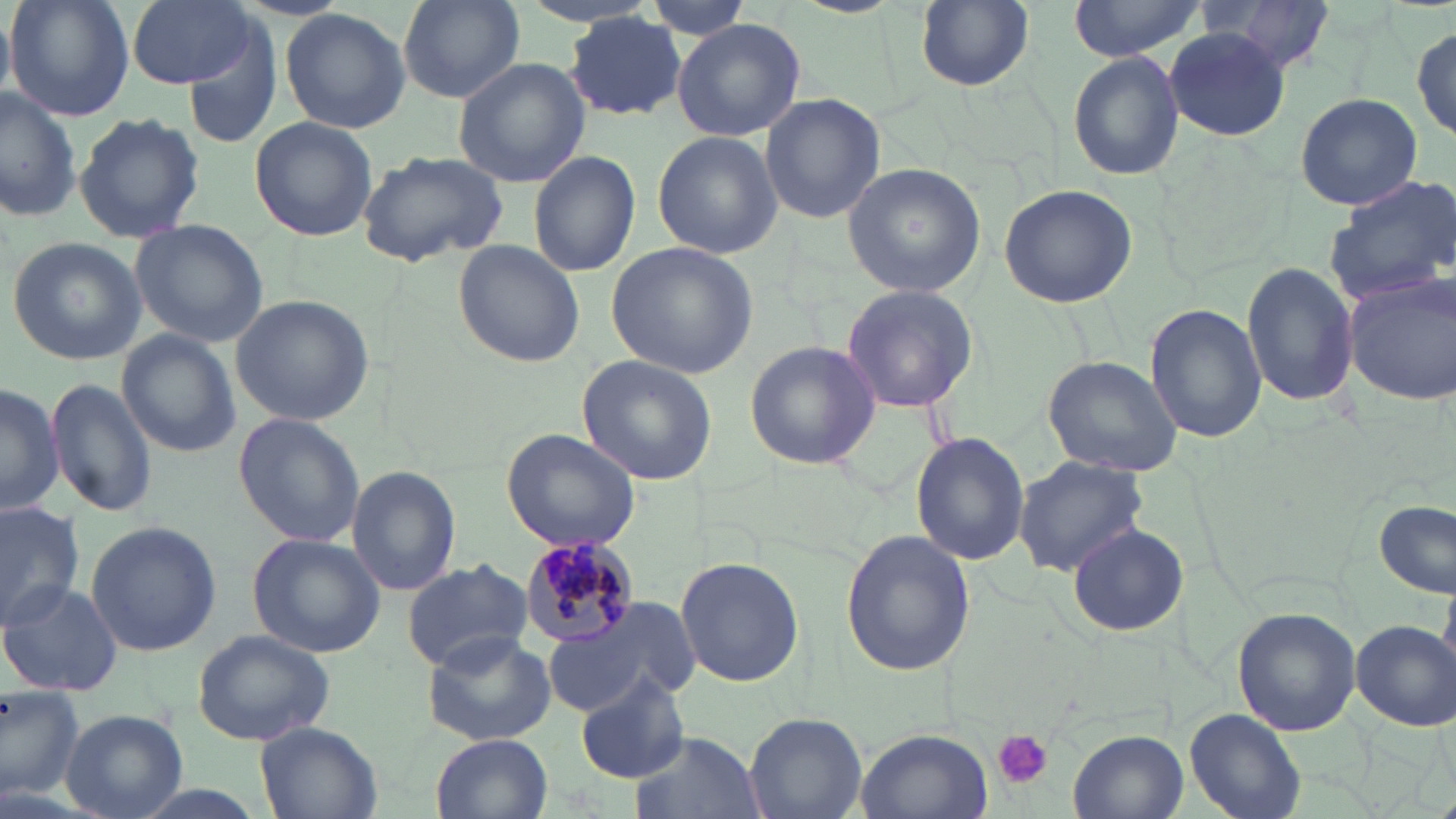
slide-level diagnosis = Plasmodium malariae
platelet locations = approximate bounding boxes as (x1,y1)-(x2,y2) corner pairs in pixels: (992,729)-(1052,787)
magnification = 1000x
Plasmodium malariae-infected red blood cell locations = approximate bounding boxes as (x1,y1)-(x2,y2) corner pairs in pixels: (515,537)-(643,647)
image size = 1456×819 pixels
stain = May-Grünwald-Giemsa
preparation = thin blood smear
uninfected red blood cell locations = approximate bounding boxes as (x1,y1)-(x2,y2) corner pairs in pixels: (6,0)-(136,122), (126,0)-(262,91), (396,0)-(528,107), (637,0)-(759,42), (1205,0)-(1339,77), (913,1)-(1036,92), (1068,1)-(1209,60), (279,7)-(413,135), (0,10)-(16,99), (564,14)-(688,121), (673,18)-(806,140), (1412,25)-(1455,146), (1165,29)-(1291,138), (180,34)-(283,147), (1066,50)-(1187,183), (453,58)-(589,187), (0,85)-(78,224), (1294,92)-(1423,210), (760,93)-(886,224), (73,111)-(204,244), (249,116)-(379,243), (653,131)-(782,258), (355,149)-(512,267), (530,151)-(641,279), (841,162)-(986,297), (1325,174)-(1456,308), (998,183)-(1136,308), (129,218)-(269,349), (7,236)-(147,365), (453,241)-(586,366), (608,242)-(758,378), (1243,262)-(1358,408), (1345,272)-(1455,404), (841,283)-(979,413), (230,293)-(375,427), (1146,304)-(1267,444), (116,327)-(240,460), (744,339)-(879,469), (578,353)-(718,485), (1041,355)-(1184,477), (45,377)-(156,517), (0,382)-(63,517), (231,413)-(367,548), (502,427)-(643,552), (911,432)-(1027,566), (1013,455)-(1148,576), (347,464)-(460,595), (1376,499)-(1454,598), (0,500)-(87,627), (83,520)-(223,655), (1067,523)-(1186,638), (840,531)-(975,675), (247,533)-(386,658), (675,556)-(804,686), (401,557)-(532,672), (0,579)-(124,697), (543,603)-(695,719), (1232,609)-(1360,734), (1352,617)-(1455,730), (190,627)-(336,747), (420,632)-(555,746), (575,669)-(690,784), (0,683)-(85,804), (60,708)-(187,819), (1185,709)-(1305,819), (744,712)-(868,818), (256,721)-(382,819), (856,728)-(992,819), (1068,730)-(1186,819), (628,731)-(766,819), (432,732)-(552,818)
modality = light microscopy
field of view = one of a larger specimen